Assess this cell for malaria.
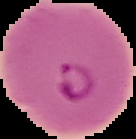

It is parasitized.

From a thin blood smear. Image is 136×139 pixels. The area outside the segmented cell region is set to black.